State which parasite is depicted.
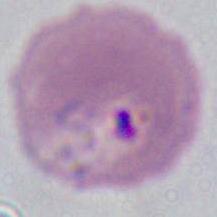

This is Plasmodium.

Photomicrograph. Captured at either 400x or 1000x magnification.